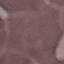
Summary:
  - Malaria status: uninfected
  - Image type: automatically extracted cell patch, resized to 64 × 64 pixels
  - Stain: Giemsa
  - Preparation: thin blood smear
  - Capture: smartphone camera at the microscope eyepiece